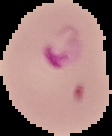
Summary:
  - Malaria status: parasitized
  - Image size: 112×136 pixels
  - Image type: segmented cell region on a black background
  - Preparation: thin blood smear